Identify the parasite.
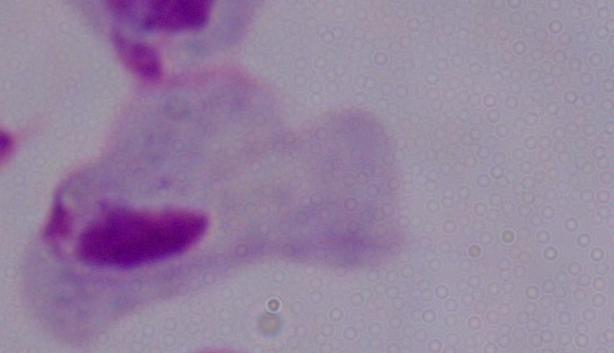

This is a trichomonad.

Micrograph. 1000x magnification.